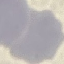

Summary:
  - Malaria status: uninfected
  - Capture: smartphone through the microscope eyepiece
  - Preparation: thin smear
  - Image type: automatically extracted cell patch, resized to 64 × 64 pixels
  - Stain: Giemsa